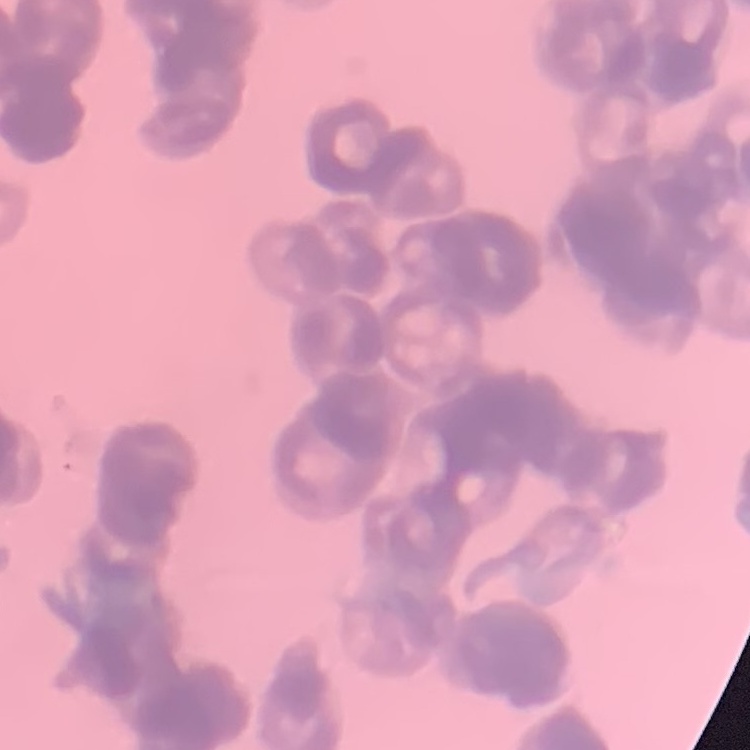
{
  "red_blood_cell_morphology": "rouleaux formation",
  "image_type": "square crop of a larger photomicrograph",
  "preparation": "thin peripheral smear",
  "stain": "Field's or Giemsa"
}